Identify the parasite.
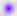
Toxoplasma gondii.

{
  "magnification": "400x",
  "modality": "photomicrograph"
}